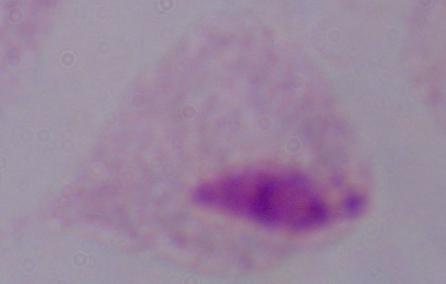
modality = micrograph
magnification = 1000x
identification = trichomonad